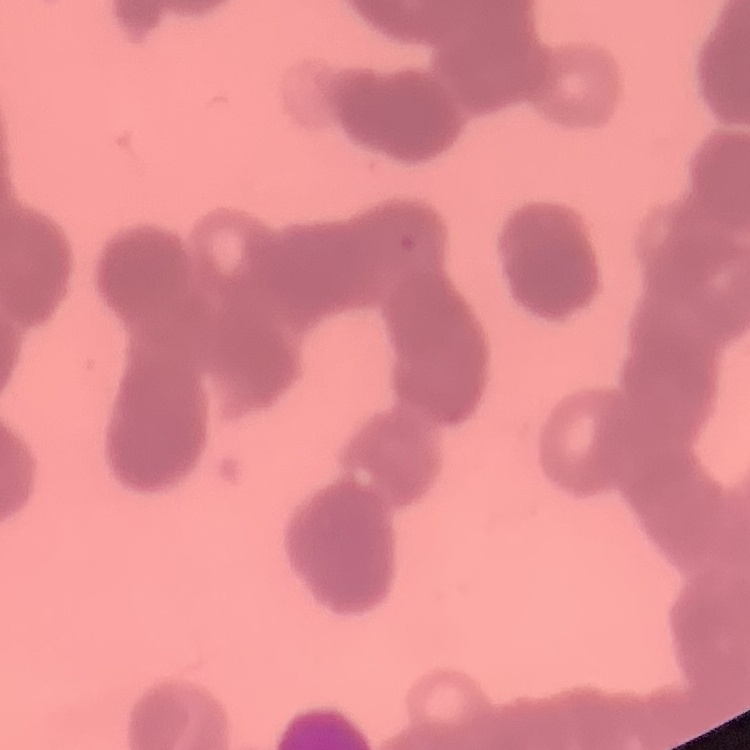

erythrocyte morphology = rouleaux formation
preparation = thin blood film
stain = Field's or Giemsa
image type = one tile cut from a larger photomicrograph